Name the blood parasite species.
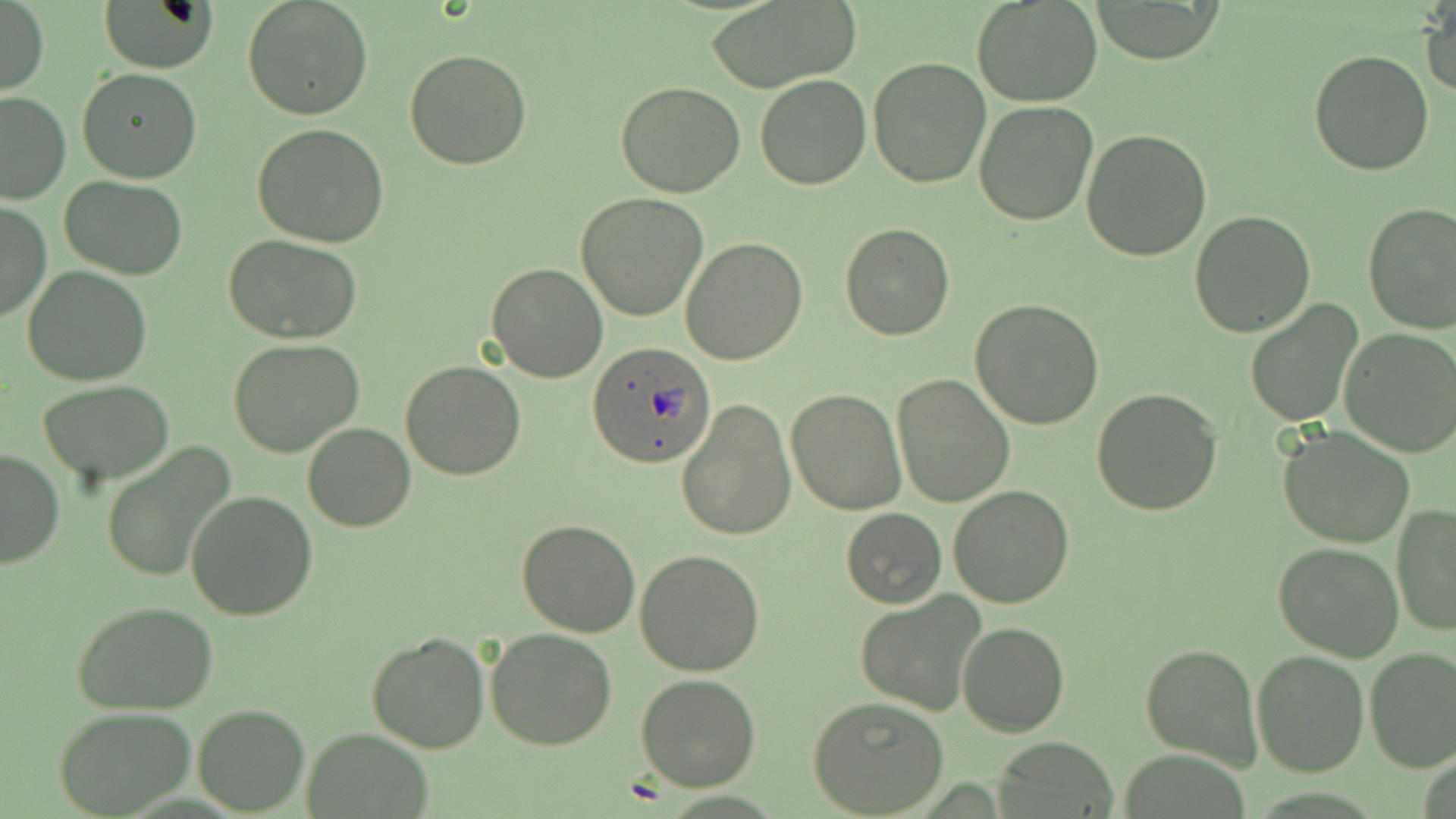
Plasmodium ovale.

Summary:
  - Coordinate format: approximate bounding boxes as named x1/y1/x2/y2 corners in pixels
  - Uninfected red blood cell locations: (x1=243, y1=0, x2=373, y2=121), (x1=973, y1=0, x2=1103, y2=106), (x1=1, y1=1, x2=48, y2=96), (x1=706, y1=1, x2=860, y2=90), (x1=1086, y1=1, x2=1226, y2=63), (x1=100, y1=2, x2=217, y2=73), (x1=1423, y1=4, x2=1455, y2=98), (x1=1309, y1=48, x2=1434, y2=176), (x1=404, y1=49, x2=532, y2=170), (x1=868, y1=56, x2=994, y2=189), (x1=78, y1=67, x2=202, y2=184), (x1=754, y1=72, x2=871, y2=189), (x1=615, y1=82, x2=747, y2=198), (x1=0, y1=90, x2=71, y2=203), (x1=974, y1=101, x2=1097, y2=226), (x1=251, y1=123, x2=390, y2=247), (x1=1082, y1=127, x2=1213, y2=262), (x1=60, y1=176, x2=188, y2=279), (x1=577, y1=191, x2=708, y2=321), (x1=1, y1=200, x2=50, y2=323), (x1=1363, y1=203, x2=1456, y2=335), (x1=1189, y1=209, x2=1315, y2=337), (x1=840, y1=223, x2=954, y2=340), (x1=223, y1=234, x2=365, y2=344), (x1=681, y1=237, x2=807, y2=365), (x1=485, y1=263, x2=609, y2=383), (x1=24, y1=266, x2=151, y2=386), (x1=971, y1=299, x2=1104, y2=428), (x1=1245, y1=301, x2=1361, y2=427), (x1=1339, y1=327, x2=1456, y2=457), (x1=229, y1=338, x2=363, y2=456), (x1=401, y1=360, x2=526, y2=481), (x1=892, y1=375, x2=1014, y2=506), (x1=37, y1=380, x2=176, y2=485), (x1=1092, y1=388, x2=1224, y2=516), (x1=786, y1=389, x2=905, y2=515), (x1=677, y1=396, x2=797, y2=541), (x1=302, y1=422, x2=415, y2=533), (x1=1277, y1=427, x2=1417, y2=551), (x1=101, y1=443, x2=236, y2=585), (x1=0, y1=447, x2=64, y2=570), (x1=948, y1=485, x2=1075, y2=607), (x1=184, y1=490, x2=317, y2=622), (x1=1391, y1=504, x2=1456, y2=637), (x1=841, y1=508, x2=946, y2=608), (x1=515, y1=519, x2=642, y2=638), (x1=1273, y1=542, x2=1404, y2=660), (x1=635, y1=550, x2=765, y2=677), (x1=856, y1=591, x2=987, y2=716), (x1=73, y1=601, x2=219, y2=715), (x1=958, y1=619, x2=1069, y2=736), (x1=485, y1=628, x2=617, y2=750), (x1=366, y1=630, x2=491, y2=753), (x1=1139, y1=642, x2=1262, y2=773), (x1=1364, y1=647, x2=1456, y2=772), (x1=1251, y1=648, x2=1369, y2=776), (x1=635, y1=673, x2=762, y2=791), (x1=806, y1=695, x2=950, y2=817), (x1=192, y1=705, x2=309, y2=814), (x1=56, y1=708, x2=195, y2=818), (x1=301, y1=727, x2=435, y2=818), (x1=994, y1=737, x2=1122, y2=816)
  - Plasmodium ovale-infected red blood cell locations: (x1=586, y1=340, x2=716, y2=467)
  - Field of view: one of a larger specimen
  - Image size: 1456×819 pixels
  - Preparation: thin blood smear
  - Modality: optical microscopy
  - Stain: May-Grünwald-Giemsa
  - Magnification: 1000x